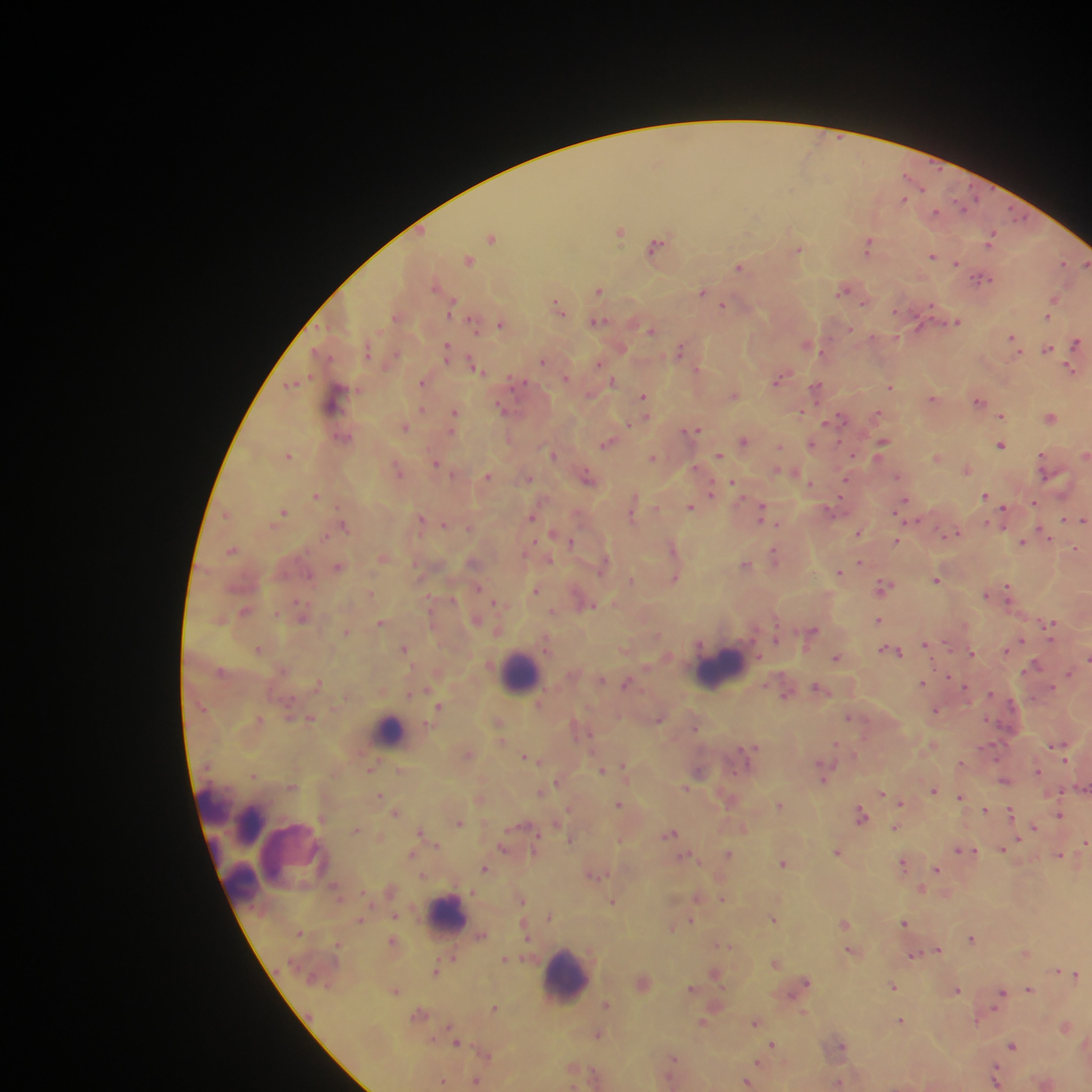
Approximate centers as x y in pixels.
Summary:
  - Malaria parasite locations: 921 189; 903 199; 963 204; 936 212; 1017 216; 620 230; 491 238; 990 240; 657 245; 869 245; 799 249; 933 256; 468 260; 956 263; 1063 263; 1086 264; 740 267; 983 278; 599 290; 842 291; 702 292; 1054 300; 865 303; 723 306; 452 307; 558 308; 897 311; 1048 316; 598 320; 957 322; 474 325; 501 325; 918 326; 850 329; 651 330; 872 337; 1012 337; 1076 343; 805 345; 622 348; 680 349; 1047 349; 369 350; 446 350; 543 361; 599 364; 475 366; 697 369; 1071 371; 566 377; 778 379; 516 381; 613 381; 422 382; 291 384; 816 387; 891 387; 734 395; 335 397; 644 397; 933 398; 979 401; 501 407; 422 410; 800 412; 878 413; 455 414; 1001 416; 837 418; 1050 418; 830 421; 629 424; 405 427; 695 430; 345 438; 744 440; 607 443; 812 443; 882 443; 1002 445; 780 446; 551 453; 288 455; 718 455; 1086 455; 653 457; 936 457; 436 463; 397 468; 967 469; 778 471; 488 477; 588 477; 897 477; 528 478; 845 482; 735 483; 811 483; 711 492; 316 495; 985 496; 634 501; 1034 503; 903 504; 690 507; 833 509; 1003 511; 283 512; 763 512; 633 513; 532 516; 421 519; 1064 520; 1083 520; 444 524; 778 524; 344 526; 469 527; 553 532; 952 533; 858 534; 1045 534; 324 536; 897 541; 573 542; 1023 543; 672 547; 1075 549; 232 550; 775 557; 860 563; 745 564; 339 566; 603 566; 839 572; 675 578; 632 579; 936 579; 883 587; 479 589; 535 590; 1008 593; 986 595; 452 598; 496 603; 589 605; 245 611; 303 616; 476 620; 878 620; 381 622; 1047 624; 347 632; 813 632; 657 635; 776 636; 1021 641; 925 645; 404 648; 1008 648; 259 649; 894 651; 972 653; 1087 657; 836 658; 1035 666; 1070 672; 601 680; 319 683; 627 683; 921 683; 964 687; 819 688; 785 694; 990 694; 539 702; 1011 703; 439 706; 936 711; 848 717; 660 718; 311 719; 695 727; 1058 746; 748 748; 468 753; 527 757; 370 769; 602 770; 1038 771; 698 772; 824 772; 254 775; 1004 780; 557 782; 292 786; 1084 788; 934 790; 541 792; 881 793; 379 795; 960 797; 901 802; 619 804; 779 804; 985 809; 397 812; 1010 812; 861 815; 1059 815; 458 822; 743 827; 896 827; 1034 827; 356 829; 671 833; 572 839; 621 839; 1085 842; 503 847; 1003 847; 963 850; 837 852; 728 853; 411 854; 687 855; 1059 855; 783 863; 903 864; 484 868; 936 869; 594 875; 922 889; 696 897; 723 899; 523 901; 612 902; 395 915; 360 919; 773 919; 691 921; 904 922; 845 923; 672 927; 481 936; 972 938; 723 945; 939 950; 851 951; 1024 952; 914 955; 505 959; 776 963; 436 971; 1057 971; 715 974; 1076 974; 805 983; 893 986; 691 988; 956 989; 1029 989; 396 991; 1001 994; 607 1004; 494 1008; 804 1012; 900 1020; 976 1021; 702 1022; 755 1023; 1065 1027; 598 1034; 457 1043; 772 1044; 1012 1045; 840 1046; 673 1059; 759 1061; 995 1076; 442 1080; 477 1082; 839 1082; 747 1083
  - Leukocyte locations: 719 666; 520 672; 389 730; 213 803; 249 824; 290 854; 240 882; 448 915; 565 975
  - Country: Ghana
  - Preparation: thick blood smear
  - Field of view: single
  - Image size: 1092×1092 pixels
  - Capture: mobile-phone photograph through a microscope